Locate every Plasmodium malariae-infected red blood cell.
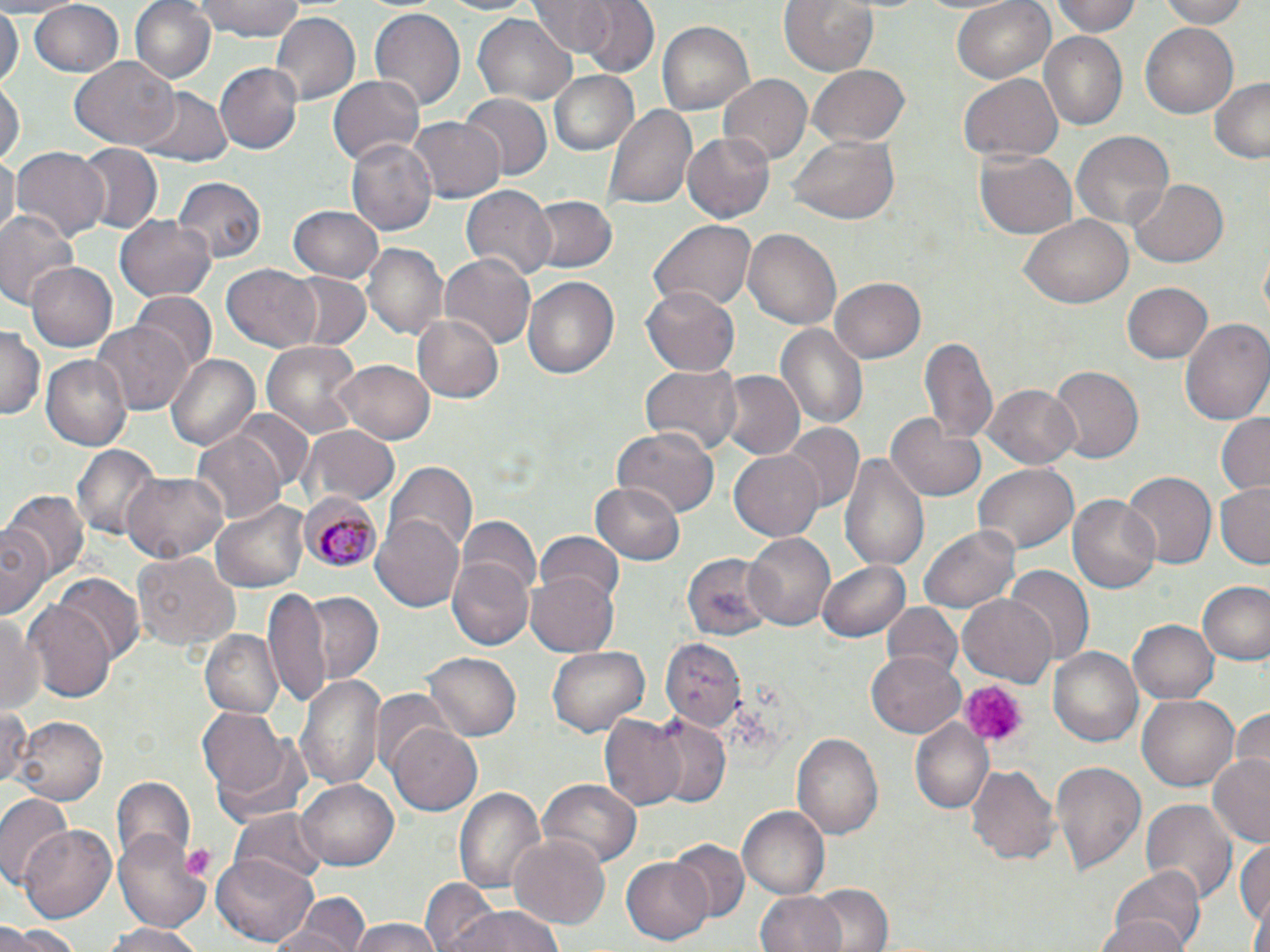
Approximate bounding boxes as named x1/y1/x2/y2 corners in pixels.
Plasmodium malariae-infected red blood cells: (x1=298, y1=493, x2=385, y2=574).

Summary:
  - Uninfected red blood cell locations: (x1=128, y1=0, x2=217, y2=86), (x1=191, y1=0, x2=309, y2=41), (x1=575, y1=0, x2=658, y2=78), (x1=779, y1=0, x2=881, y2=79), (x1=951, y1=0, x2=1055, y2=85), (x1=1053, y1=0, x2=1141, y2=36), (x1=1153, y1=0, x2=1251, y2=27), (x1=528, y1=1, x2=614, y2=56), (x1=28, y1=2, x2=124, y2=77), (x1=0, y1=3, x2=22, y2=89), (x1=369, y1=7, x2=466, y2=113), (x1=268, y1=12, x2=359, y2=107), (x1=471, y1=14, x2=577, y2=106), (x1=657, y1=19, x2=754, y2=114), (x1=1140, y1=22, x2=1240, y2=119), (x1=1041, y1=34, x2=1126, y2=128), (x1=71, y1=57, x2=179, y2=150), (x1=216, y1=62, x2=304, y2=154), (x1=806, y1=65, x2=911, y2=150), (x1=549, y1=70, x2=638, y2=155), (x1=958, y1=72, x2=1064, y2=163), (x1=328, y1=74, x2=424, y2=168), (x1=718, y1=74, x2=812, y2=165), (x1=1208, y1=78, x2=1270, y2=165), (x1=0, y1=80, x2=22, y2=172), (x1=136, y1=85, x2=232, y2=169), (x1=459, y1=93, x2=553, y2=181), (x1=605, y1=101, x2=695, y2=212), (x1=409, y1=117, x2=503, y2=203), (x1=1070, y1=132, x2=1175, y2=233), (x1=682, y1=133, x2=774, y2=221), (x1=344, y1=137, x2=436, y2=238), (x1=788, y1=139, x2=900, y2=224), (x1=75, y1=142, x2=160, y2=234), (x1=10, y1=147, x2=109, y2=245), (x1=975, y1=150, x2=1077, y2=240), (x1=0, y1=151, x2=18, y2=242), (x1=173, y1=176, x2=266, y2=263), (x1=1129, y1=178, x2=1229, y2=270), (x1=465, y1=184, x2=556, y2=282), (x1=528, y1=195, x2=618, y2=273), (x1=288, y1=205, x2=384, y2=283), (x1=0, y1=212, x2=79, y2=313), (x1=1020, y1=214, x2=1132, y2=310), (x1=117, y1=215, x2=217, y2=303), (x1=649, y1=219, x2=758, y2=313), (x1=743, y1=227, x2=842, y2=332), (x1=363, y1=243, x2=448, y2=341), (x1=439, y1=253, x2=535, y2=350), (x1=25, y1=261, x2=117, y2=354), (x1=222, y1=262, x2=322, y2=352), (x1=283, y1=272, x2=372, y2=353), (x1=521, y1=275, x2=622, y2=382), (x1=830, y1=278, x2=926, y2=363), (x1=1122, y1=281, x2=1213, y2=365), (x1=642, y1=286, x2=740, y2=376), (x1=131, y1=292, x2=216, y2=373), (x1=411, y1=312, x2=505, y2=404), (x1=1181, y1=318, x2=1270, y2=428), (x1=774, y1=321, x2=869, y2=434), (x1=92, y1=322, x2=191, y2=413), (x1=0, y1=327, x2=42, y2=420), (x1=919, y1=333, x2=1001, y2=449), (x1=261, y1=339, x2=364, y2=443), (x1=165, y1=354, x2=259, y2=452), (x1=41, y1=355, x2=131, y2=451), (x1=331, y1=360, x2=435, y2=444), (x1=641, y1=362, x2=740, y2=457), (x1=1048, y1=366, x2=1144, y2=465), (x1=715, y1=371, x2=803, y2=461), (x1=980, y1=384, x2=1079, y2=470), (x1=230, y1=410, x2=317, y2=495), (x1=887, y1=411, x2=986, y2=504), (x1=1215, y1=411, x2=1270, y2=497), (x1=779, y1=423, x2=863, y2=515), (x1=299, y1=426, x2=398, y2=508), (x1=611, y1=427, x2=723, y2=517), (x1=192, y1=432, x2=287, y2=521), (x1=70, y1=444, x2=158, y2=540), (x1=729, y1=448, x2=826, y2=542), (x1=839, y1=451, x2=931, y2=576), (x1=386, y1=462, x2=476, y2=554), (x1=974, y1=464, x2=1079, y2=555), (x1=124, y1=472, x2=227, y2=560), (x1=1121, y1=472, x2=1216, y2=573), (x1=1214, y1=481, x2=1270, y2=568), (x1=592, y1=483, x2=686, y2=563), (x1=5, y1=490, x2=87, y2=581), (x1=1068, y1=494, x2=1163, y2=595), (x1=211, y1=499, x2=311, y2=593), (x1=372, y1=511, x2=466, y2=614), (x1=458, y1=517, x2=539, y2=600), (x1=2, y1=520, x2=52, y2=620), (x1=919, y1=525, x2=1021, y2=611), (x1=534, y1=531, x2=624, y2=608), (x1=742, y1=532, x2=835, y2=632), (x1=132, y1=550, x2=237, y2=651), (x1=680, y1=553, x2=773, y2=641), (x1=816, y1=558, x2=910, y2=643), (x1=448, y1=561, x2=532, y2=650), (x1=1004, y1=566, x2=1092, y2=666), (x1=525, y1=570, x2=619, y2=657), (x1=55, y1=575, x2=143, y2=661), (x1=1196, y1=581, x2=1270, y2=667), (x1=266, y1=588, x2=332, y2=709), (x1=298, y1=591, x2=385, y2=686), (x1=958, y1=593, x2=1057, y2=688), (x1=24, y1=598, x2=114, y2=700), (x1=881, y1=603, x2=962, y2=681), (x1=0, y1=607, x2=43, y2=718), (x1=1127, y1=619, x2=1218, y2=705), (x1=203, y1=631, x2=281, y2=718), (x1=660, y1=637, x2=745, y2=730), (x1=1051, y1=644, x2=1142, y2=749), (x1=546, y1=645, x2=651, y2=738), (x1=867, y1=650, x2=964, y2=736), (x1=421, y1=651, x2=519, y2=743), (x1=298, y1=672, x2=385, y2=791), (x1=1136, y1=692, x2=1238, y2=795), (x1=1235, y1=706, x2=1270, y2=774), (x1=0, y1=708, x2=33, y2=788), (x1=198, y1=708, x2=292, y2=799), (x1=598, y1=712, x2=688, y2=812), (x1=646, y1=715, x2=732, y2=809), (x1=12, y1=716, x2=106, y2=806), (x1=910, y1=720, x2=995, y2=815), (x1=387, y1=721, x2=484, y2=816), (x1=792, y1=732, x2=883, y2=841), (x1=211, y1=735, x2=316, y2=834), (x1=1207, y1=753, x2=1270, y2=851), (x1=1050, y1=760, x2=1145, y2=879), (x1=965, y1=763, x2=1060, y2=866), (x1=538, y1=777, x2=642, y2=871), (x1=109, y1=778, x2=196, y2=866), (x1=296, y1=778, x2=400, y2=871), (x1=455, y1=787, x2=545, y2=894), (x1=0, y1=791, x2=72, y2=888), (x1=1139, y1=798, x2=1237, y2=907), (x1=738, y1=807, x2=829, y2=901), (x1=232, y1=808, x2=328, y2=890), (x1=17, y1=821, x2=118, y2=921), (x1=113, y1=825, x2=210, y2=931), (x1=507, y1=832, x2=610, y2=929), (x1=1236, y1=835, x2=1270, y2=936), (x1=668, y1=838, x2=749, y2=921), (x1=210, y1=854, x2=319, y2=947), (x1=622, y1=857, x2=716, y2=943), (x1=1103, y1=866, x2=1206, y2=952), (x1=423, y1=879, x2=503, y2=952), (x1=807, y1=885, x2=896, y2=952), (x1=755, y1=892, x2=850, y2=952), (x1=278, y1=895, x2=369, y2=951), (x1=443, y1=902, x2=567, y2=952), (x1=1093, y1=914, x2=1189, y2=952), (x1=346, y1=917, x2=445, y2=952), (x1=102, y1=922, x2=205, y2=952), (x1=1, y1=926, x2=84, y2=952)
  - Platelet locations: (x1=957, y1=679, x2=1025, y2=747)
  - Slide-level diagnosis: Plasmodium malariae
  - Stain: May-Grünwald-Giemsa
  - Modality: light microscopy
  - Field of view: one of a larger specimen
  - Preparation: thin blood smear
  - Image size: 1270×952 pixels
  - Magnification: 1000x